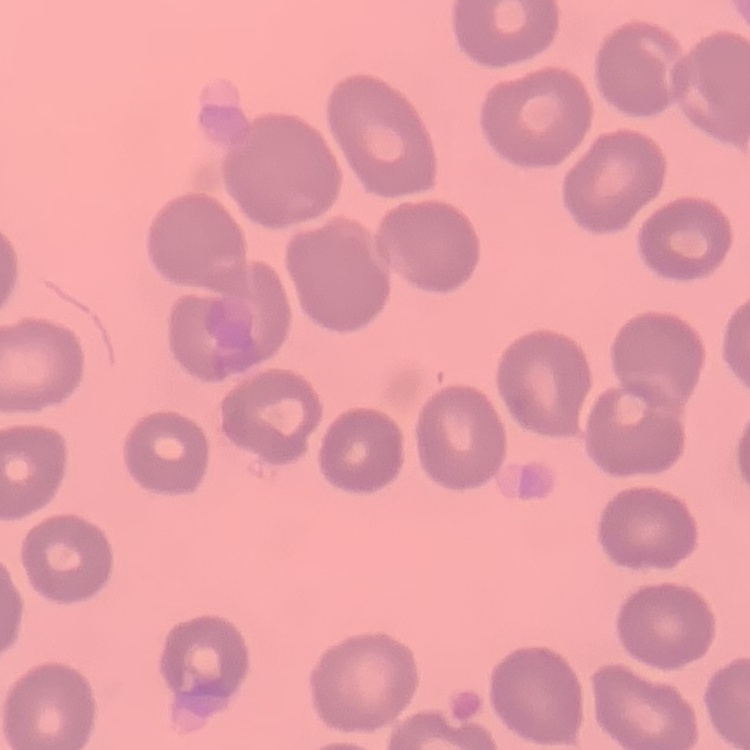

erythrocyte morphology = no rouleaux formation
image type = square crop of a larger photomicrograph
preparation = thin blood smear
stain = Field's or Giemsa